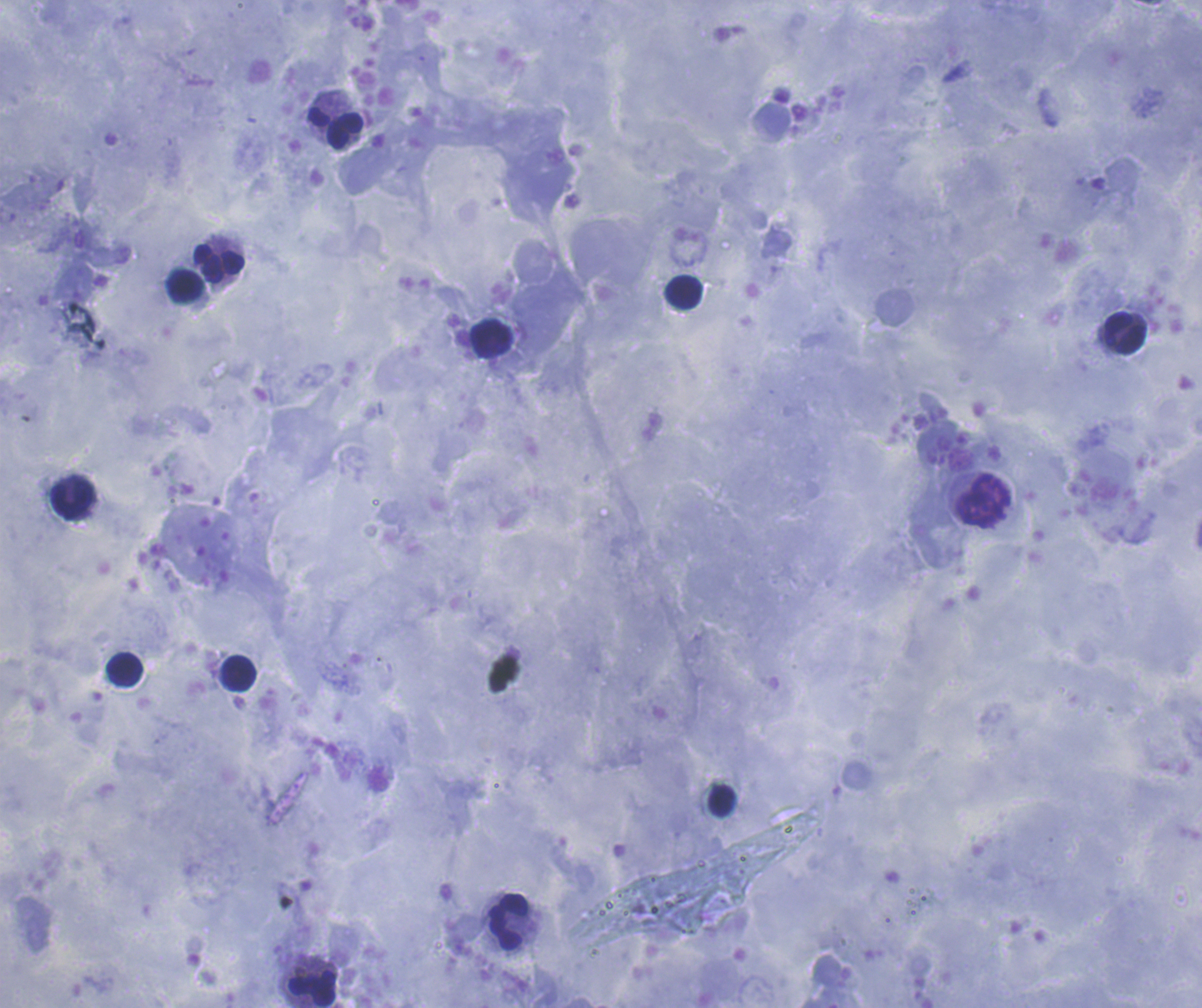

Approximate centers as (x, y) in pixels.
Summary:
  - Leukocyte locations: (335, 128), (218, 263), (186, 285), (684, 291), (1124, 333), (492, 338), (71, 497), (983, 500), (125, 670), (238, 673), (722, 801), (508, 921), (311, 987)
  - Context: previously used in an actual diagnosis
  - Stain: Romanowsky
  - Result: no Plasmodium parasites seen
  - Magnification: 100x
  - Field of view: one from this slide
  - Image size: 1202×1008 pixels
  - Preparation: thick smear of blood
  - Coloration quality: good
  - Background quality: satisfactory